Classify this cell by malaria status.
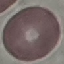

Uninfected.

Summary:
  - Image type: cell patch, automatically extracted from a larger field of view and resized to 64 × 64 pixels
  - Stain: Giemsa
  - Preparation: thin blood smear
  - Capture: smartphone through the microscope eyepiece